Point out each malaria parasite.
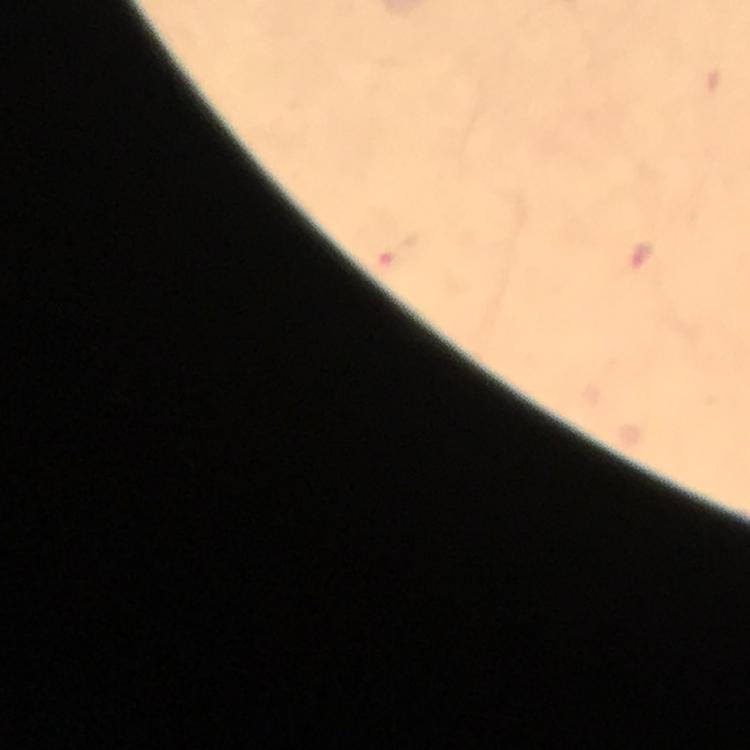
Approximate centers as [x, y] in pixels.
Malaria parasites: [400, 251], [641, 260].

preparation = thick blood smear
cropped from = one field of view
image size = 750×750 pixels
immersion oil = used
magnification = 100x
context = from a diagnostic examination for malaria
capture = smartphone photograph through a microscope
stain = Giemsa